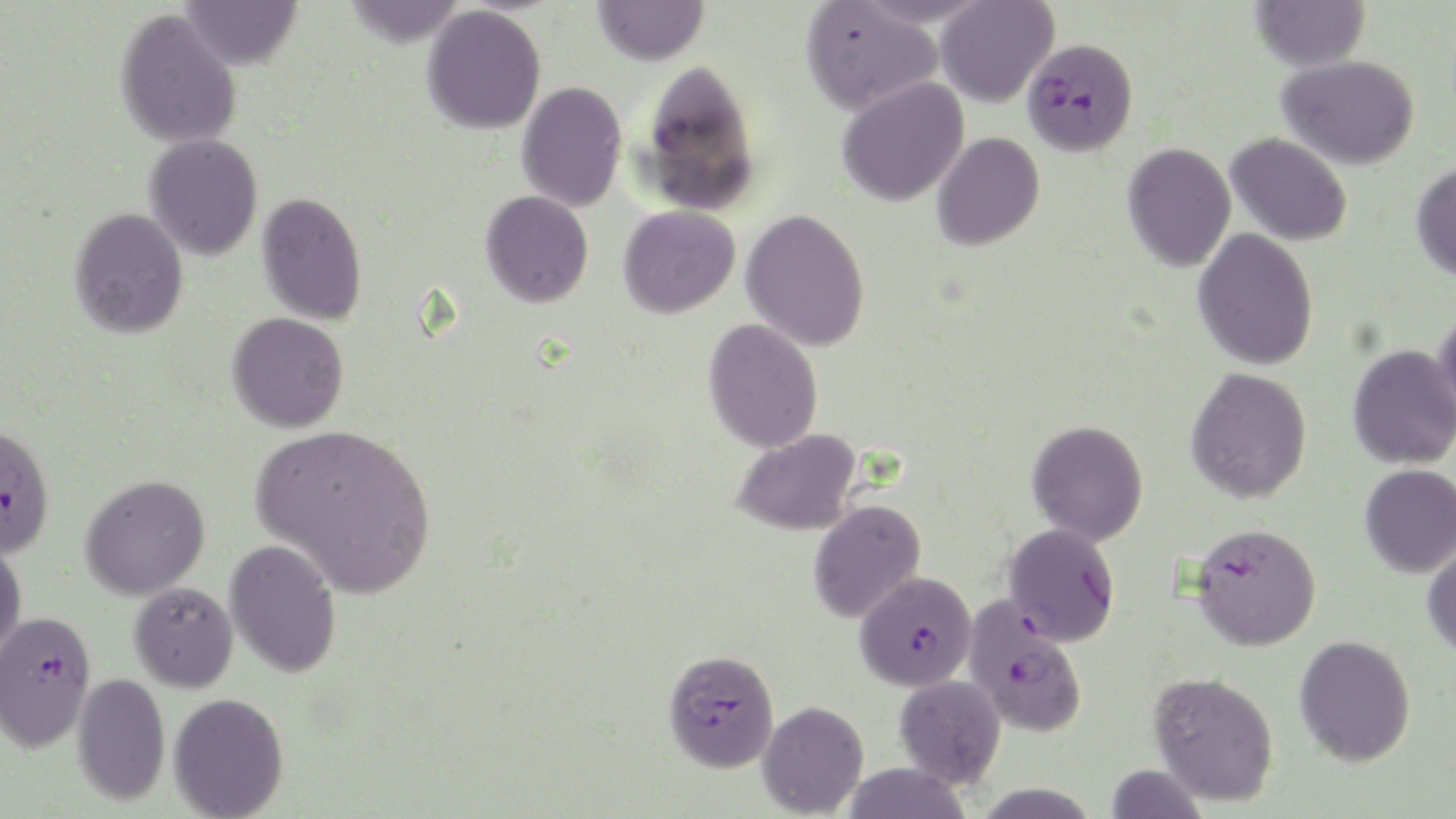

slide-level diagnosis = Plasmodium falciparum
uninfected red blood cell locations = approximate bounding boxes as (x1, y1, x2, y2) in pixels: (178, 0, 303, 71), (593, 0, 709, 66), (1249, 0, 1371, 72), (934, 1, 1058, 108), (800, 2, 943, 116), (422, 6, 546, 134), (114, 8, 243, 149), (1277, 55, 1419, 169), (638, 57, 761, 216), (837, 76, 970, 206), (516, 81, 627, 212), (931, 133, 1045, 251), (1225, 133, 1353, 246), (144, 134, 263, 260), (1122, 142, 1236, 272), (1411, 160, 1456, 281), (480, 190, 594, 308), (256, 191, 368, 326), (618, 205, 740, 319), (69, 207, 189, 339), (740, 209, 870, 352), (1193, 228, 1319, 370), (1433, 305, 1456, 427), (226, 312, 349, 434), (703, 318, 824, 453), (1347, 344, 1456, 470), (1185, 367, 1313, 504), (1026, 419, 1149, 546), (253, 421, 437, 599), (730, 429, 864, 536), (1359, 464, 1456, 577), (79, 473, 210, 601), (807, 499, 926, 623), (0, 539, 27, 664), (224, 539, 342, 678), (1422, 540, 1456, 658), (129, 582, 238, 692), (1294, 634, 1416, 766), (1148, 671, 1280, 806), (72, 673, 170, 805), (893, 674, 1006, 788), (168, 692, 289, 819), (756, 700, 869, 817), (841, 763, 972, 819), (1104, 763, 1207, 818)
Plasmodium falciparum-infected red blood cell locations = approximate bounding boxes as (x1, y1, x2, y2) in pixels: (1022, 37, 1138, 156), (0, 424, 55, 558), (1003, 522, 1121, 647), (1190, 522, 1322, 651), (855, 571, 977, 691), (962, 597, 1089, 738), (0, 609, 98, 753), (662, 648, 779, 772)
stain = May-Grünwald-Giemsa
image size = 1456×819 pixels
field of view = single
magnification = 1000x
modality = optical microscopy
preparation = thin blood smear